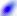
magnification: 400x
modality: photomicrograph
identification: Toxoplasma gondii